Outline each Plasmodium falciparum-infected red blood cell.
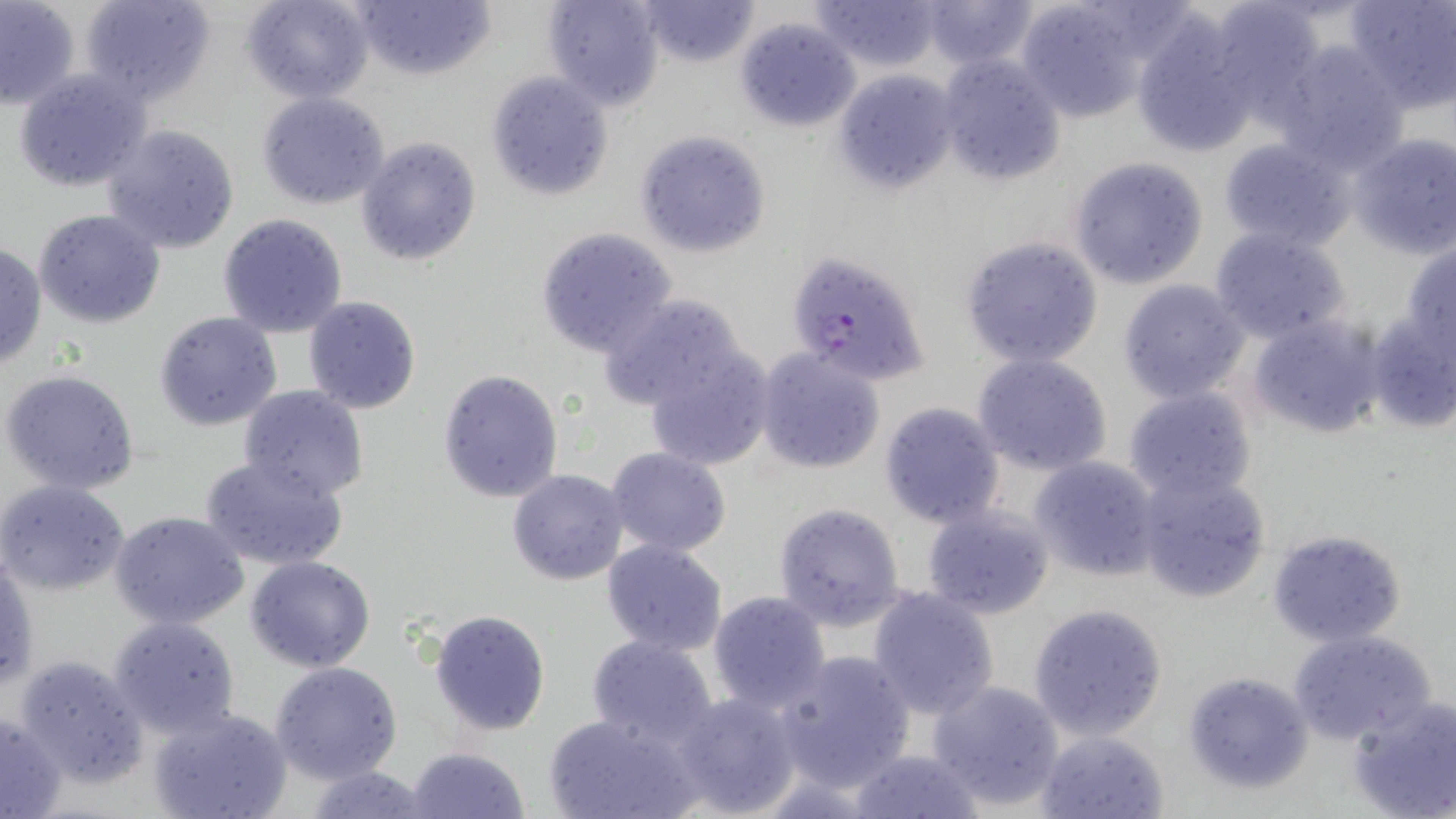

Approximate bounding boxes as named x1/y1/x2/y2 corners in pixels.
Plasmodium falciparum-infected red blood cells: (x1=788, y1=252, x2=930, y2=389).

slide-level diagnosis = Plasmodium falciparum
image size = 1456×819 pixels
field of view = one of a larger specimen
uninfected red blood cell locations = approximate bounding boxes as named x1/y1/x2/y2 corners in pixels: (x1=0, y1=0, x2=82, y2=109), (x1=78, y1=0, x2=218, y2=106), (x1=241, y1=0, x2=374, y2=103), (x1=349, y1=0, x2=496, y2=82), (x1=541, y1=0, x2=666, y2=111), (x1=632, y1=0, x2=762, y2=69), (x1=809, y1=0, x2=945, y2=73), (x1=916, y1=0, x2=1042, y2=68), (x1=1204, y1=0, x2=1324, y2=112), (x1=1345, y1=0, x2=1455, y2=115), (x1=1014, y1=2, x2=1150, y2=122), (x1=735, y1=15, x2=861, y2=132), (x1=1130, y1=17, x2=1257, y2=159), (x1=1272, y1=40, x2=1410, y2=171), (x1=936, y1=53, x2=1067, y2=186), (x1=13, y1=68, x2=149, y2=194), (x1=834, y1=70, x2=960, y2=195), (x1=485, y1=72, x2=615, y2=202), (x1=255, y1=92, x2=391, y2=210), (x1=102, y1=124, x2=241, y2=255), (x1=634, y1=130, x2=772, y2=258), (x1=1348, y1=132, x2=1456, y2=259), (x1=355, y1=135, x2=483, y2=267), (x1=1216, y1=136, x2=1358, y2=253), (x1=1068, y1=157, x2=1208, y2=289), (x1=33, y1=208, x2=166, y2=330), (x1=216, y1=213, x2=348, y2=338), (x1=1209, y1=225, x2=1353, y2=346), (x1=534, y1=227, x2=677, y2=358), (x1=961, y1=235, x2=1105, y2=370), (x1=1400, y1=240, x2=1456, y2=354), (x1=0, y1=243, x2=47, y2=370), (x1=1117, y1=279, x2=1251, y2=405), (x1=597, y1=291, x2=759, y2=421), (x1=302, y1=296, x2=421, y2=415), (x1=153, y1=310, x2=283, y2=431), (x1=1365, y1=312, x2=1455, y2=432), (x1=1247, y1=314, x2=1386, y2=440), (x1=636, y1=335, x2=779, y2=474), (x1=754, y1=346, x2=886, y2=474), (x1=972, y1=352, x2=1113, y2=475), (x1=436, y1=368, x2=564, y2=505), (x1=2, y1=369, x2=141, y2=495), (x1=238, y1=384, x2=368, y2=501), (x1=1123, y1=389, x2=1258, y2=503), (x1=877, y1=401, x2=1006, y2=530), (x1=605, y1=447, x2=733, y2=559), (x1=198, y1=456, x2=351, y2=571), (x1=1027, y1=456, x2=1162, y2=583), (x1=507, y1=468, x2=631, y2=586), (x1=1134, y1=469, x2=1272, y2=604), (x1=0, y1=479, x2=131, y2=597), (x1=773, y1=501, x2=908, y2=632), (x1=921, y1=504, x2=1056, y2=621), (x1=110, y1=511, x2=250, y2=630), (x1=1266, y1=528, x2=1408, y2=648), (x1=601, y1=538, x2=729, y2=657), (x1=1, y1=554, x2=38, y2=694), (x1=245, y1=555, x2=375, y2=673), (x1=865, y1=587, x2=1001, y2=718), (x1=707, y1=590, x2=831, y2=713), (x1=1029, y1=603, x2=1169, y2=741), (x1=427, y1=608, x2=551, y2=737), (x1=108, y1=616, x2=240, y2=739), (x1=1290, y1=629, x2=1437, y2=745), (x1=586, y1=634, x2=720, y2=746), (x1=776, y1=650, x2=916, y2=792), (x1=14, y1=654, x2=150, y2=788), (x1=270, y1=662, x2=403, y2=784), (x1=1181, y1=670, x2=1312, y2=794), (x1=927, y1=679, x2=1066, y2=810), (x1=670, y1=690, x2=802, y2=818), (x1=1347, y1=695, x2=1456, y2=819), (x1=147, y1=705, x2=293, y2=819), (x1=0, y1=710, x2=66, y2=818), (x1=544, y1=710, x2=704, y2=819), (x1=1036, y1=729, x2=1170, y2=819), (x1=402, y1=746, x2=531, y2=819), (x1=848, y1=748, x2=986, y2=819), (x1=305, y1=765, x2=434, y2=819)
magnification = 1000x
preparation = thin blood film
modality = light microscopy
stain = May-Grünwald-Giemsa